State which parasite is depicted.
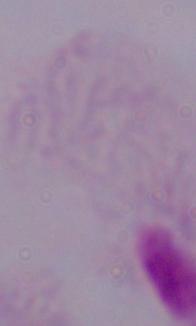
This is a trichomonad.

modality = photomicrograph
magnification = 1000x